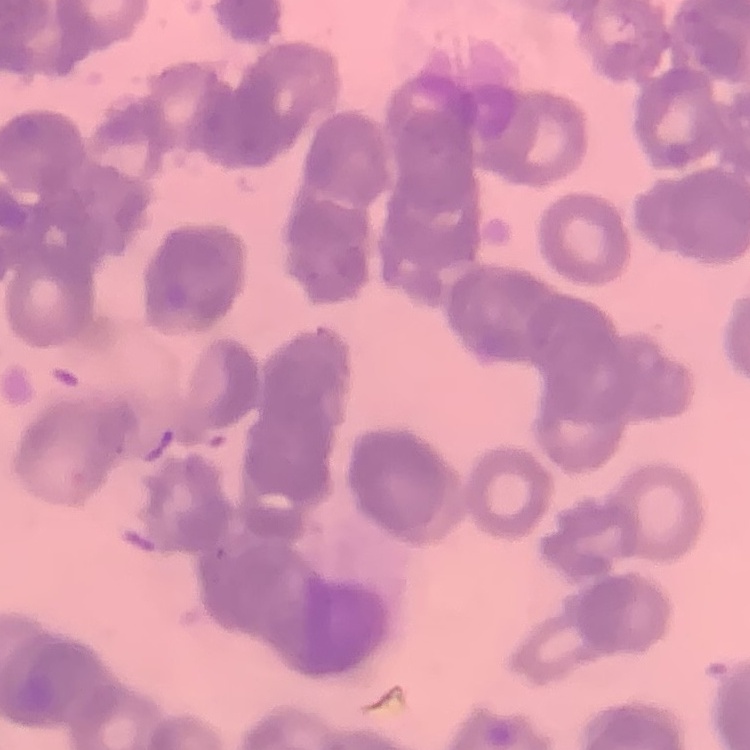 The erythrocytes exhibit rouleaux formation. Stained with either Field's or Giemsa. Square crop of a larger photomicrograph. Thin blood smear.